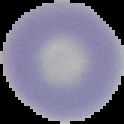

preparation = thin blood smear
image type = segmented cell region with the area outside set to black
malaria status = uninfected
image size = 124×124 pixels